Identify the blood parasite species.
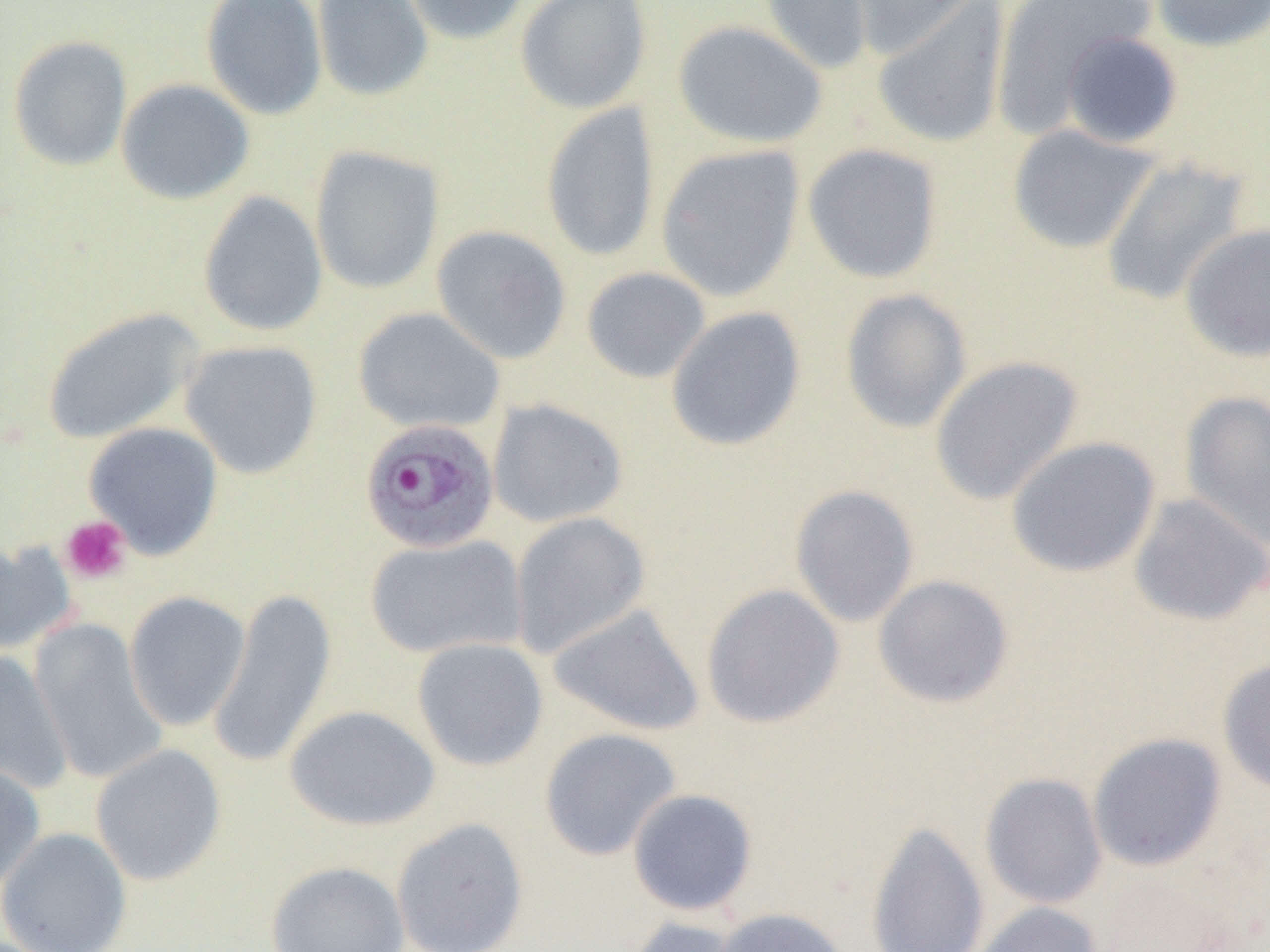

Plasmodium ovale.

platelet locations = approximate bounding boxes as (x1,y1)-(x2,y2) corner pairs in pixels: (60,515)-(131,584)
preparation = thin blood smear
magnification = 1000x
image size = 1270×952 pixels
field of view = one of a larger specimen
uninfected red blood cell locations = approximate bounding boxes as (x1,y1)-(x2,y2) corner pairs in pixels: (201,0)-(328,120), (311,0)-(434,102), (398,0)-(532,46), (515,0)-(652,114), (758,0)-(874,76), (844,0)-(989,60), (990,0)-(1159,137), (1150,0)-(1270,53), (871,2)-(1012,149), (673,19)-(828,149), (1059,31)-(1183,148), (7,35)-(133,171), (116,78)-(255,205), (540,101)-(661,263), (1006,124)-(1160,254), (802,143)-(943,284), (655,144)-(805,302), (310,145)-(444,294), (1099,156)-(1252,307), (198,191)-(328,337), (431,224)-(573,364), (1179,224)-(1270,363), (581,266)-(711,383), (840,289)-(973,433), (666,306)-(807,452), (42,307)-(205,444), (352,307)-(506,434), (179,339)-(323,479), (930,355)-(1084,505), (1179,391)-(1270,549), (487,398)-(628,528), (83,422)-(224,559), (1006,436)-(1161,579), (789,484)-(920,627), (1128,493)-(1269,626), (509,511)-(651,659), (365,534)-(527,659), (0,539)-(77,656), (872,574)-(1015,709), (700,583)-(845,729), (208,588)-(338,769), (123,591)-(251,731), (548,603)-(705,737), (28,618)-(167,785), (412,637)-(549,771), (1,649)-(72,794), (1218,657)-(1270,795), (284,704)-(440,831), (538,727)-(682,861), (1088,732)-(1227,872), (90,743)-(227,886), (0,759)-(46,891), (979,772)-(1108,909), (627,788)-(758,916), (390,817)-(530,952), (865,820)-(990,952), (0,827)-(133,952), (266,860)-(410,952), (972,902)-(1102,952), (711,907)-(851,952), (622,916)-(749,952)
modality = optical microscopy
Plasmodium ovale-infected red blood cell locations = approximate bounding boxes as (x1,y1)-(x2,y2) corner pairs in pixels: (359,417)-(501,554)